Report the malaria status of this cell.
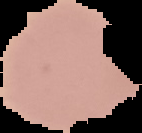
It is uninfected.

Summary:
  - Image size: 142×133 pixels
  - Preparation: thin blood smear
  - Image type: cell region segmented out of the field of view; surrounding area masked to black